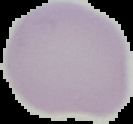
Result: no malaria parasites detected. Cell region segmented out of the field of view; the surrounding area is masked to black. Image is 133×124 pixels. From a thin blood film.